Report the malaria status of this cell.
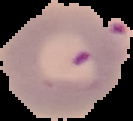
It is parasitized.

preparation = thin blood smear
image type = cell region segmented out of the field of view; surrounding area masked to black
image size = 133×121 pixels